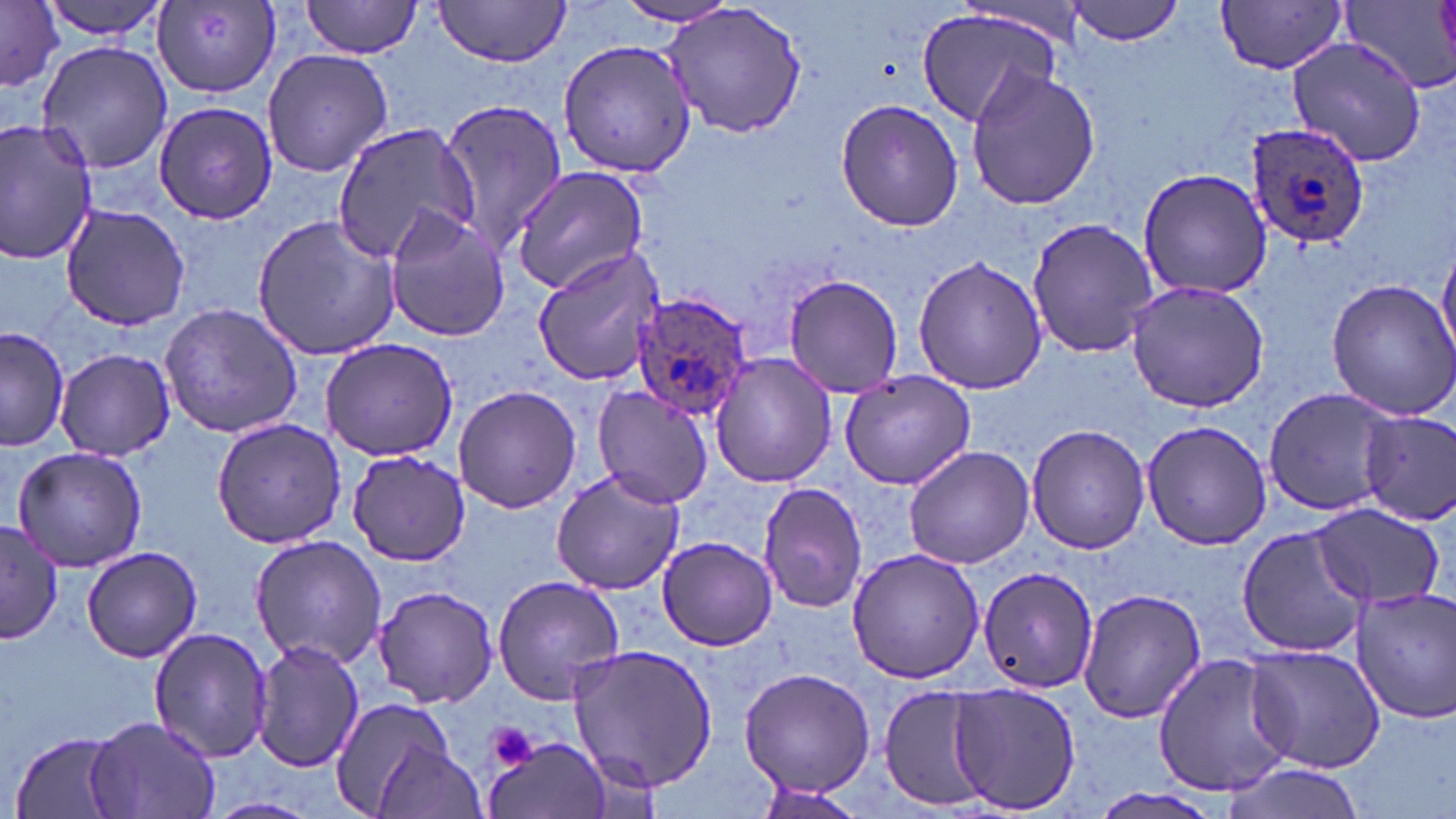

Plasmodium ovale-infected red blood cell locations = approximate bounding boxes as [x1, y1, x2, y2] in pixels: [1243, 119, 1371, 249], [628, 291, 755, 422]
slide-level diagnosis = Plasmodium ovale
image size = 1456×819 pixels
stain = May-Grünwald-Giemsa
platelet locations = approximate bounding boxes as [x1, y1, x2, y2] in pixels: [483, 721, 541, 774]
preparation = thin blood smear
field of view = single
modality = optical microscopy
magnification = 1000x
uninfected red blood cell locations = approximate bounding boxes as [x1, y1, x2, y2] in pixels: [1, 0, 63, 90], [37, 0, 174, 39], [299, 0, 425, 59], [432, 0, 573, 67], [611, 0, 743, 27], [658, 0, 810, 141], [1067, 0, 1188, 46], [1216, 1, 1350, 73], [153, 2, 281, 97], [1338, 3, 1456, 98], [915, 7, 1064, 129], [1284, 36, 1429, 170], [557, 38, 697, 177], [35, 40, 175, 175], [260, 48, 392, 177], [965, 66, 1101, 211], [837, 97, 964, 233], [438, 98, 566, 255], [154, 102, 277, 224], [0, 119, 97, 266], [332, 121, 482, 262], [509, 166, 649, 295], [1138, 168, 1275, 300], [61, 203, 190, 331], [383, 207, 511, 341], [249, 214, 402, 360], [1027, 218, 1159, 360], [1437, 246, 1456, 367], [531, 247, 664, 385], [912, 254, 1050, 395], [782, 274, 904, 398], [1125, 277, 1272, 414], [1325, 279, 1456, 420], [160, 303, 304, 437], [1, 326, 69, 452], [319, 337, 458, 461], [56, 348, 175, 459], [710, 353, 838, 488], [838, 370, 976, 491], [590, 382, 714, 510], [453, 384, 583, 514], [1263, 389, 1400, 516], [1360, 411, 1456, 526], [211, 417, 346, 549], [1141, 420, 1273, 550], [1026, 423, 1149, 555], [9, 444, 150, 573], [901, 445, 1034, 569], [347, 449, 472, 566], [551, 467, 684, 596], [756, 481, 868, 615], [1309, 502, 1446, 612], [1, 521, 62, 643], [1235, 525, 1370, 660], [250, 534, 385, 669], [656, 536, 778, 650], [81, 545, 203, 664], [846, 548, 988, 685], [979, 568, 1100, 694], [492, 576, 625, 703], [372, 584, 499, 708], [1349, 584, 1456, 723], [1076, 588, 1206, 724], [147, 626, 274, 764], [252, 640, 365, 774], [1245, 642, 1388, 774], [568, 644, 719, 791], [1152, 652, 1294, 799], [740, 667, 877, 794], [946, 683, 1081, 815], [876, 689, 985, 808], [327, 697, 454, 814], [87, 717, 224, 819], [9, 730, 130, 818], [483, 735, 614, 819], [375, 738, 488, 819], [1218, 761, 1369, 818], [749, 784, 869, 819], [1088, 788, 1223, 819], [203, 795, 323, 819]